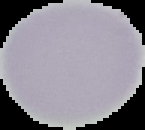

{
  "image_type": "segmented cell region with the area outside set to black",
  "preparation": "thin blood smear",
  "image_size": "145×130 pixels",
  "malaria_status": "uninfected"
}